Name the blood parasite species.
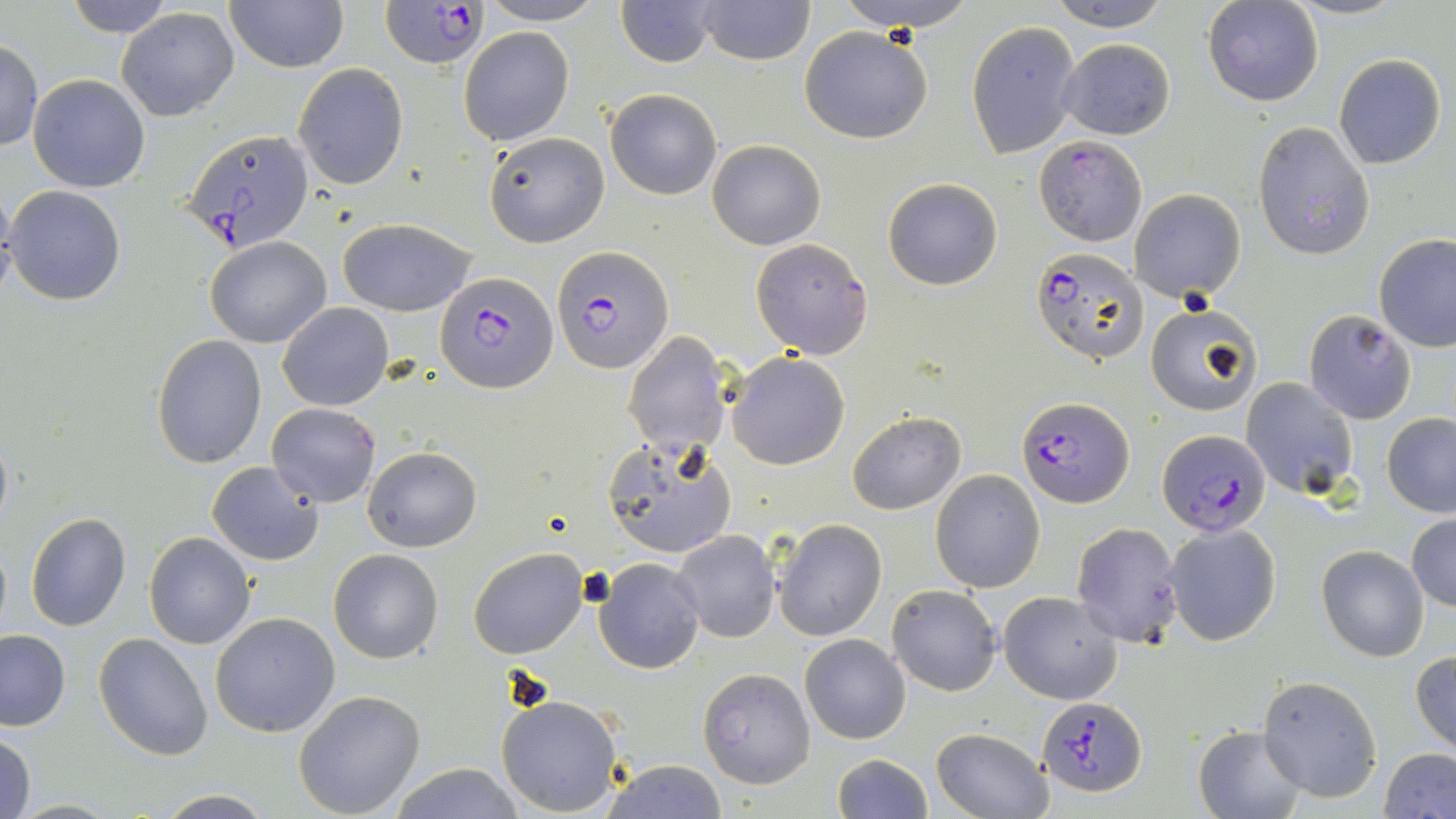

Plasmodium falciparum.

Approximate bounding boxes as [x1, y1, x2, y2] in pixels. Uninfected red blood cell locations: [223, 0, 348, 71], [477, 0, 606, 26], [616, 0, 717, 67], [696, 0, 814, 66], [836, 0, 974, 30], [1044, 0, 1175, 31], [1284, 0, 1405, 21], [60, 1, 181, 38], [1202, 1, 1324, 108], [116, 7, 239, 122], [966, 20, 1080, 159], [799, 25, 934, 144], [458, 26, 574, 147], [1057, 38, 1176, 140], [0, 39, 43, 150], [1333, 53, 1447, 170], [294, 63, 408, 189], [29, 73, 151, 193], [606, 88, 721, 200], [1253, 122, 1375, 260], [482, 129, 610, 248], [708, 139, 825, 250], [882, 176, 1003, 290], [5, 185, 126, 304], [1130, 189, 1247, 301], [337, 217, 477, 316], [1375, 234, 1456, 352], [205, 237, 329, 348], [278, 303, 394, 412], [1145, 306, 1261, 415], [1302, 309, 1417, 424], [624, 330, 736, 457], [152, 334, 267, 468], [726, 351, 850, 470], [1240, 376, 1360, 499], [265, 401, 381, 508], [847, 411, 966, 514], [1382, 413, 1456, 518], [604, 438, 736, 562], [363, 446, 481, 552], [206, 461, 325, 566], [931, 469, 1046, 593], [24, 511, 131, 631], [1407, 512, 1456, 612], [773, 518, 887, 641], [1069, 521, 1183, 646], [1164, 523, 1281, 646], [672, 530, 781, 643], [144, 533, 256, 649], [1316, 544, 1430, 663], [469, 547, 588, 659], [329, 548, 444, 665], [593, 557, 706, 674], [886, 583, 1002, 697], [999, 591, 1124, 705], [211, 612, 341, 738], [0, 630, 70, 731], [95, 631, 214, 760], [800, 634, 912, 744], [1410, 652, 1456, 755], [697, 668, 814, 788], [1256, 674, 1383, 803], [292, 690, 425, 817], [495, 694, 624, 817], [1193, 726, 1306, 819], [930, 727, 1053, 819], [1, 729, 37, 819], [1380, 748, 1456, 819], [829, 753, 933, 819], [599, 759, 730, 818], [385, 763, 528, 819], [148, 790, 280, 817]. Plasmodium falciparum-infected red blood cell locations: [383, 0, 487, 69], [181, 130, 316, 253], [1034, 137, 1148, 246], [751, 240, 871, 356], [552, 247, 674, 375], [1031, 247, 1148, 363], [435, 272, 561, 393], [1019, 398, 1132, 507], [1155, 428, 1270, 538], [1036, 697, 1145, 794]. 1000x magnification. One field of a larger specimen. Thin blood film. Optical microscopy. May-Grünwald-Giemsa-stained preparation. Image is 1456×819 pixels.